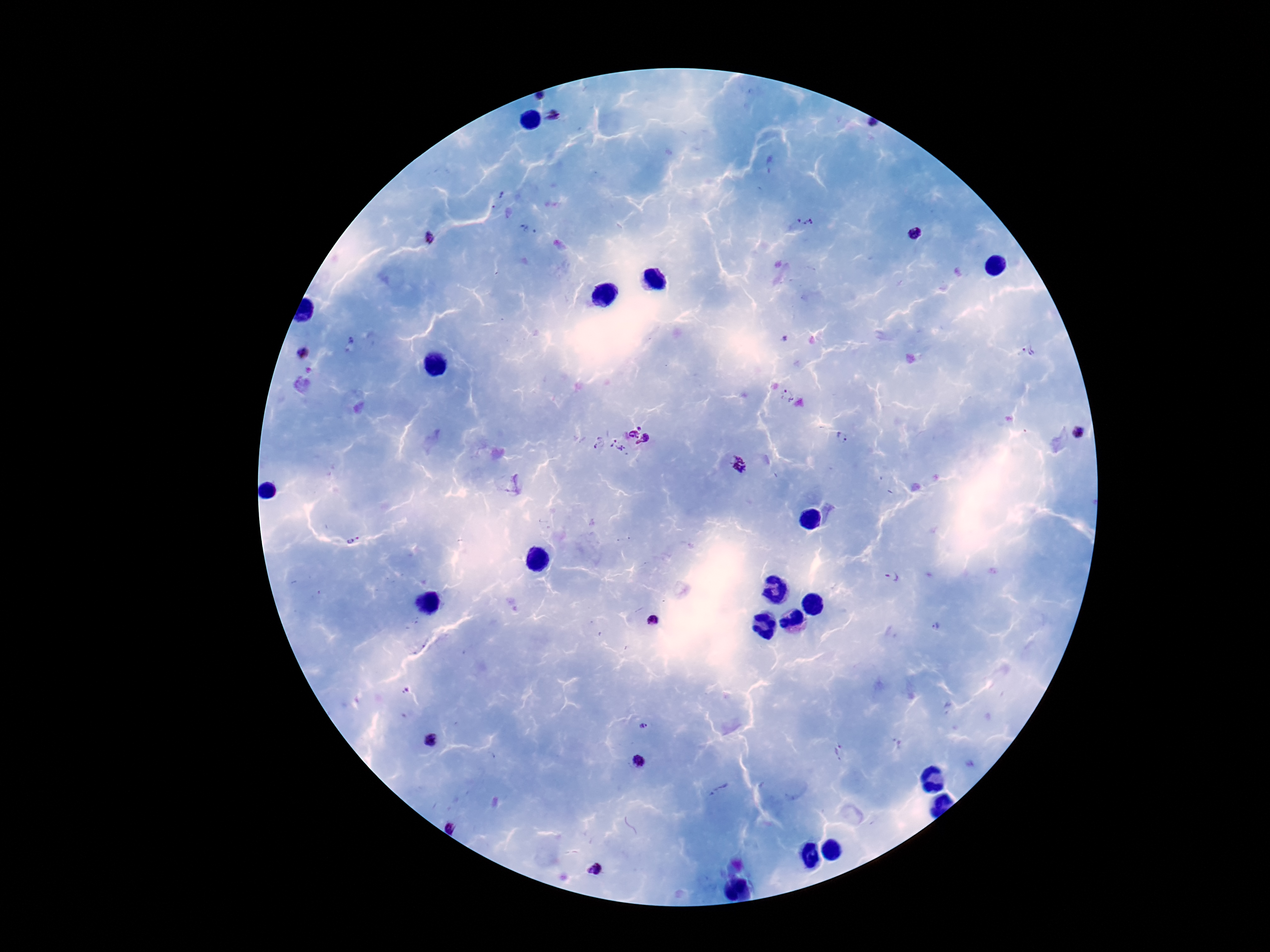
Approximate centers as [x, y] in pixels. Plasmodium parasite locations: [540, 96], [555, 116], [872, 125], [497, 201], [805, 220], [528, 229], [914, 233], [430, 238], [1030, 351], [303, 354], [786, 395], [642, 425], [1079, 431], [632, 434], [842, 436], [646, 441], [597, 442], [615, 448], [738, 464], [352, 540], [892, 577], [654, 619], [936, 627], [644, 727], [430, 741], [840, 752], [639, 762], [718, 789], [452, 825], [594, 870]. Thick blood smear. Photographed through the microscope eyepiece with a smartphone camera. Image is 1270×952 pixels. Giemsa-stained preparation. Single field of view. 100x magnification. Patient malaria status: positive.